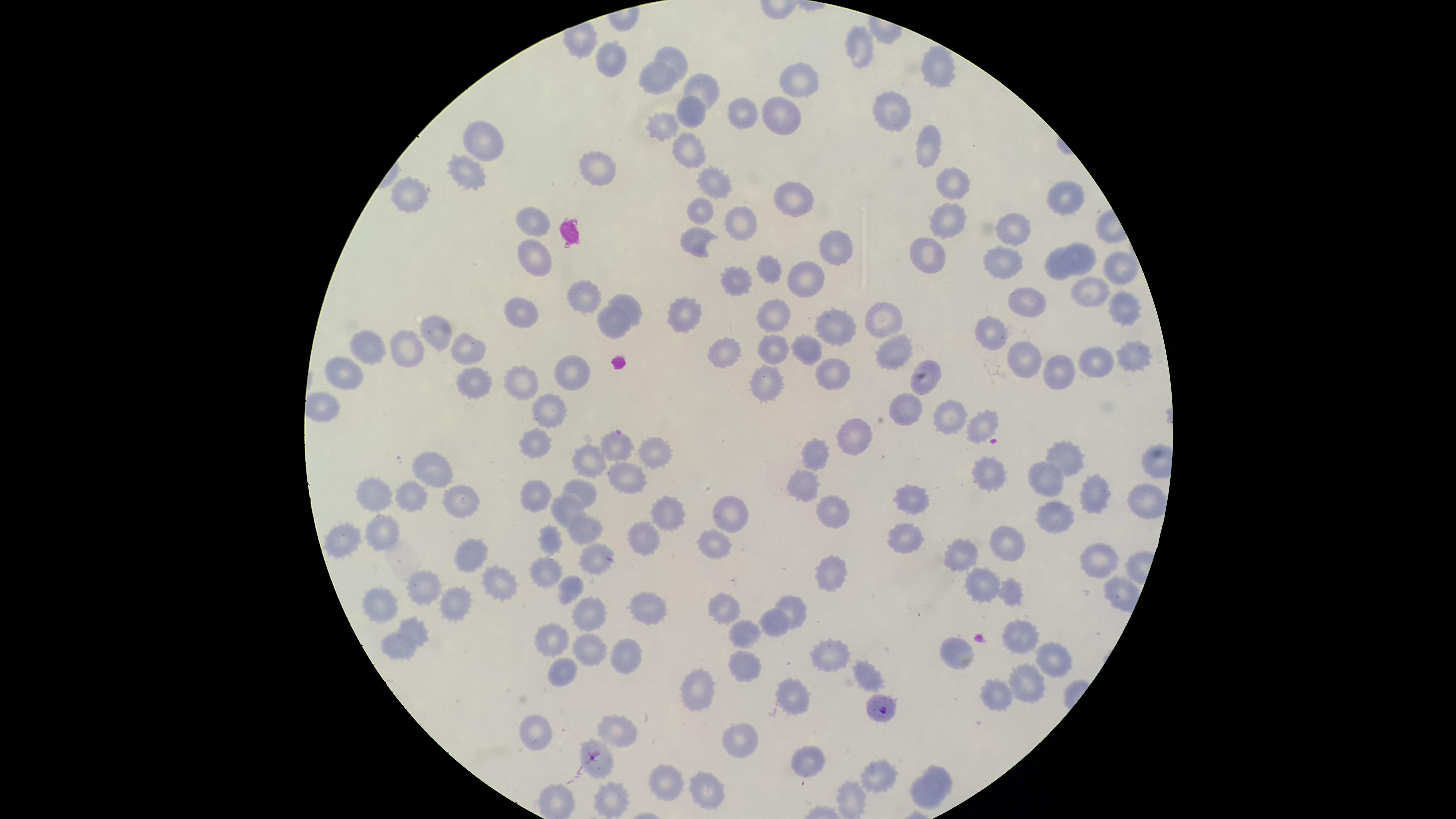
Approximate bounding boxes as {left, top, right, bottom} in pixels.
Summary:
  - Parasitized red blood cells: {598, 428, 635, 464}, {865, 691, 898, 724}
  - Uninfected red blood cells: {845, 25, 875, 68}, {595, 39, 627, 77}, {652, 47, 686, 83}, {920, 47, 956, 88}, {638, 62, 676, 96}, {780, 62, 818, 97}, {682, 72, 719, 111}, {873, 91, 911, 131}, {676, 96, 705, 127}, {761, 96, 801, 135}, {727, 97, 756, 129}, {645, 110, 680, 140}, {463, 121, 502, 160}, {916, 124, 941, 168}, {672, 131, 704, 169}, {578, 151, 615, 185}, {445, 153, 487, 192}, {697, 165, 731, 198}, {935, 165, 970, 200}, {392, 178, 425, 209}, {1045, 180, 1084, 214}, {774, 182, 813, 217}, {687, 198, 713, 223}, {929, 203, 967, 239}, {518, 206, 549, 235}, {724, 206, 757, 238}, {995, 213, 1030, 245}, {680, 229, 717, 257}, {819, 229, 853, 267}, {909, 237, 946, 273}, {518, 240, 550, 276}, {1058, 242, 1096, 275}, {982, 245, 1022, 279}, {1044, 246, 1080, 280}, {1103, 252, 1138, 285}, {756, 255, 781, 284}, {787, 261, 824, 298}, {720, 266, 750, 294}, {1071, 276, 1110, 307}, {567, 282, 600, 312}, {1007, 286, 1046, 318}, {1109, 291, 1140, 326}, {609, 294, 640, 325}, {668, 297, 701, 331}, {503, 298, 538, 326}, {757, 298, 790, 333}, {864, 302, 903, 337}, {598, 306, 628, 336}, {814, 307, 856, 347}, {975, 316, 1007, 351}, {420, 317, 450, 351}, {389, 330, 422, 367}, {350, 332, 384, 364}, {758, 334, 789, 366}, {452, 335, 485, 363}, {791, 335, 822, 365}, {875, 335, 913, 370}, {1117, 337, 1153, 372}, {709, 338, 741, 368}, {1007, 340, 1042, 378}, {1079, 346, 1114, 378}, {1043, 353, 1075, 390}, {553, 355, 590, 389}, {324, 357, 361, 390}, {815, 358, 851, 390}, {911, 360, 942, 395}, {749, 364, 784, 401}, {503, 366, 537, 399}, {457, 368, 490, 397}, {532, 393, 567, 429}, {889, 393, 922, 427}, {933, 400, 967, 437}, {967, 409, 999, 445}, {837, 418, 873, 455}, {519, 427, 551, 460}, {638, 435, 673, 469}, {801, 438, 831, 471}, {1045, 439, 1085, 478}, {573, 445, 607, 479}, {411, 450, 452, 487}, {972, 455, 1006, 493}, {1028, 460, 1064, 497}, {609, 462, 648, 494}, {788, 469, 821, 502}, {1080, 474, 1111, 514}, {355, 476, 393, 512}, {562, 479, 598, 510}, {395, 480, 428, 511}, {521, 480, 551, 513}, {1127, 482, 1165, 519}, {894, 484, 929, 516}, {441, 486, 479, 518}, {552, 494, 588, 528}, {817, 494, 850, 529}, {651, 495, 686, 532}, {714, 495, 749, 532}, {1037, 500, 1074, 533}, {364, 514, 399, 551}, {567, 514, 604, 546}, {627, 521, 660, 556}, {323, 522, 361, 557}, {888, 522, 922, 553}, {539, 523, 562, 555}, {990, 525, 1025, 562}, {699, 528, 731, 560}, {455, 538, 489, 572}, {944, 539, 977, 572}, {580, 543, 614, 574}, {1082, 544, 1119, 577}, {529, 556, 562, 588}, {817, 556, 850, 591}, {482, 565, 518, 601}, {965, 567, 1000, 602}, {408, 570, 443, 606}, {559, 575, 583, 605}, {999, 579, 1023, 607}, {362, 587, 399, 625}, {439, 587, 471, 621}, {631, 591, 667, 626}, {708, 593, 741, 624}, {774, 594, 806, 630}, {572, 596, 607, 631}, {759, 606, 790, 638}, {398, 616, 429, 648}, {730, 620, 761, 648}, {1002, 620, 1038, 655}, {535, 623, 568, 657}, {382, 630, 418, 662}, {573, 633, 607, 668}, {610, 638, 642, 675}, {940, 638, 975, 670}, {810, 640, 850, 672}, {1034, 642, 1072, 678}, {727, 650, 762, 682}, {547, 657, 578, 687}, {853, 661, 885, 692}, {1008, 663, 1045, 703}, {681, 669, 715, 713}, {776, 676, 810, 715}, {982, 679, 1012, 711}, {520, 715, 551, 752}, {597, 715, 638, 749}, {723, 723, 759, 759}, {580, 740, 613, 778}, {792, 746, 826, 776}, {862, 759, 897, 793}, {923, 765, 953, 795}, {649, 766, 683, 801}, {690, 771, 725, 811}, {909, 776, 946, 811}, {594, 781, 628, 817}, {837, 781, 866, 817}
  - Species: Plasmodium falciparum
  - Preparation: thin blood film
  - Visible region: circular
  - Field of view: single
  - Image size: 1456×819 pixels
  - Capture: smartphone photograph through the microscope eyepiece
  - Stain: Giemsa
  - Presence: malaria parasites identified